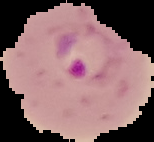
Summary:
  - Image type: segmented cell region on a black background
  - Preparation: thin blood smear
  - Malaria status: parasitized
  - Image size: 154×142 pixels